Locate platelets.
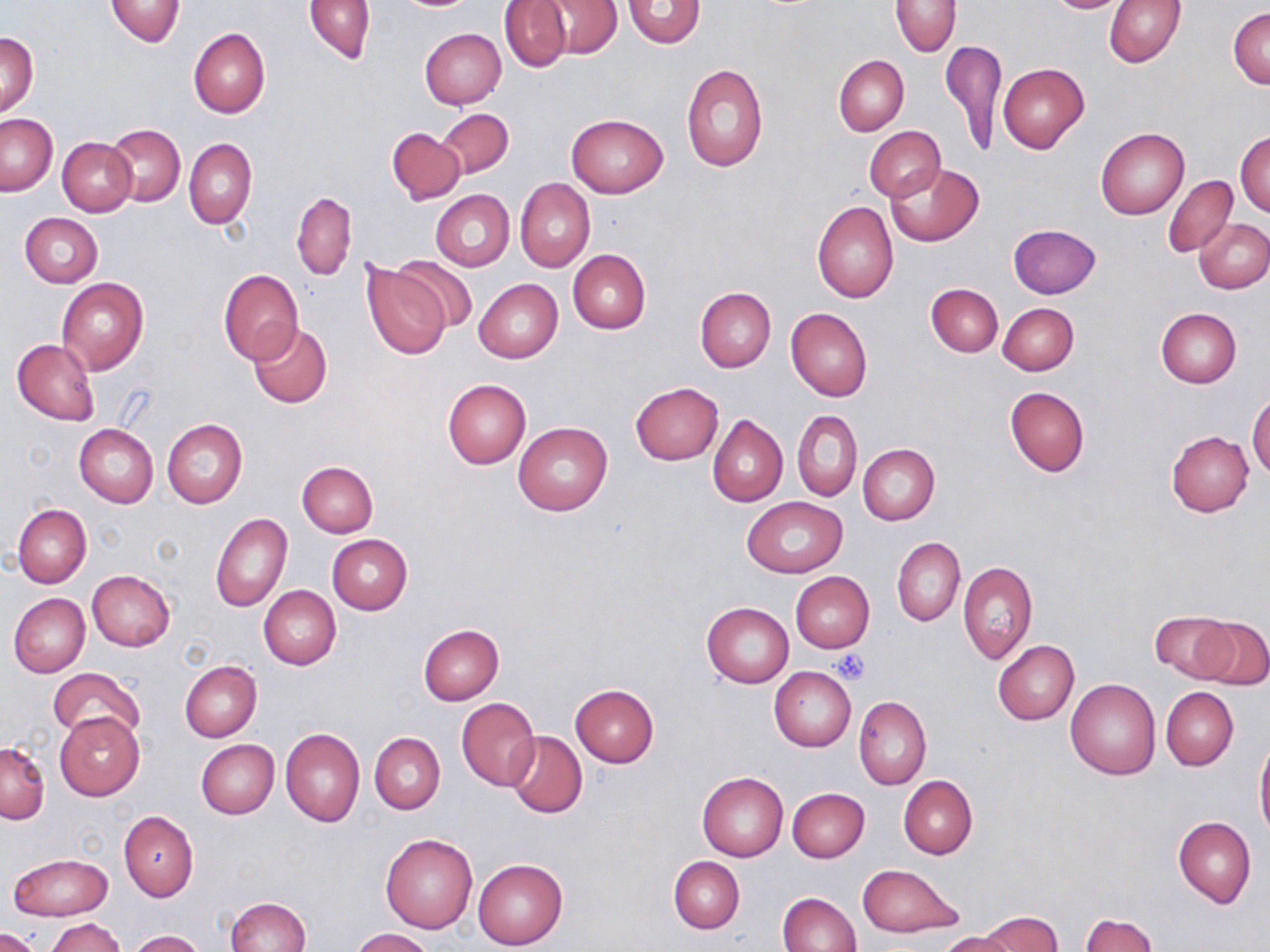

Approximate bounding boxes as (x1,y1)-(x2,y2) corner pairs in pixels.
Platelets: (832,647)-(871,685).

Summary:
  - Uninfected red blood cell locations: (105,0)-(186,46), (304,0)-(376,65), (892,0)-(959,55), (1043,0)-(1131,14), (499,1)-(572,72), (540,1)-(622,58), (623,1)-(704,48), (1104,1)-(1185,67), (1229,7)-(1270,89), (188,27)-(270,118), (419,28)-(506,108), (2,33)-(38,115), (942,41)-(1005,156), (834,55)-(908,135), (999,62)-(1089,154), (681,64)-(768,172), (437,109)-(513,178), (1,114)-(57,195), (567,114)-(667,197), (106,125)-(185,205), (387,126)-(466,205), (864,126)-(945,202), (1096,128)-(1189,218), (1235,130)-(1270,215), (58,138)-(137,216), (184,139)-(257,229), (887,162)-(984,247), (1162,176)-(1238,257), (515,178)-(595,272), (431,189)-(514,272), (291,191)-(355,281), (813,200)-(899,303), (306,202)-(387,296), (20,212)-(103,287), (1195,219)-(1270,294), (1008,223)-(1101,298), (568,249)-(651,333), (393,254)-(478,331), (361,262)-(454,360), (218,270)-(303,364), (56,277)-(149,376), (474,279)-(563,363), (926,282)-(1003,357), (695,286)-(776,372), (928,294)-(1076,366), (997,302)-(1078,375), (786,306)-(872,401), (1155,307)-(1242,387), (248,323)-(332,409), (12,339)-(99,426), (442,379)-(532,468), (630,382)-(724,465), (1004,386)-(1089,477), (1248,393)-(1270,480), (794,410)-(862,501), (708,415)-(788,506), (161,419)-(248,509), (513,422)-(612,516), (74,424)-(158,508), (1167,431)-(1254,515), (858,443)-(941,524), (296,461)-(378,537), (743,496)-(847,578), (12,503)-(91,587), (210,512)-(292,612), (327,534)-(411,616), (892,537)-(964,625), (957,562)-(1037,665), (87,570)-(175,651), (790,571)-(874,653), (259,586)-(340,670), (9,593)-(90,676), (702,601)-(793,688), (1151,611)-(1236,681), (1197,617)-(1270,691), (418,624)-(505,705), (993,640)-(1079,725), (179,661)-(261,742), (769,666)-(856,752), (49,668)-(145,744), (1065,678)-(1160,780), (569,685)-(659,767), (1162,687)-(1238,769), (854,696)-(931,789), (456,697)-(540,790), (55,712)-(144,800), (280,728)-(365,827), (507,731)-(587,818), (370,732)-(445,814), (1255,735)-(1269,841), (196,739)-(280,819), (0,743)-(49,824), (697,772)-(788,861), (899,776)-(977,858), (787,788)-(869,861), (119,812)-(199,901), (1173,815)-(1257,907), (380,834)-(478,933), (9,854)-(113,920), (669,855)-(744,933), (473,858)-(569,950), (858,864)-(961,938), (778,891)-(862,952), (224,897)-(310,952), (979,911)-(1062,952), (1079,913)-(1157,951), (45,918)-(126,952), (350,928)-(434,952), (2,930)-(41,952), (128,930)-(204,952), (938,932)-(1018,952)
  - Slide-level diagnosis: negative for blood parasites
  - Field of view: single
  - Preparation: thin blood film
  - Magnification: 1000x
  - Stain: May-Grünwald-Giemsa
  - Modality: optical microscopy
  - Image size: 1270×952 pixels